Locate every blood parasite and identify its species.
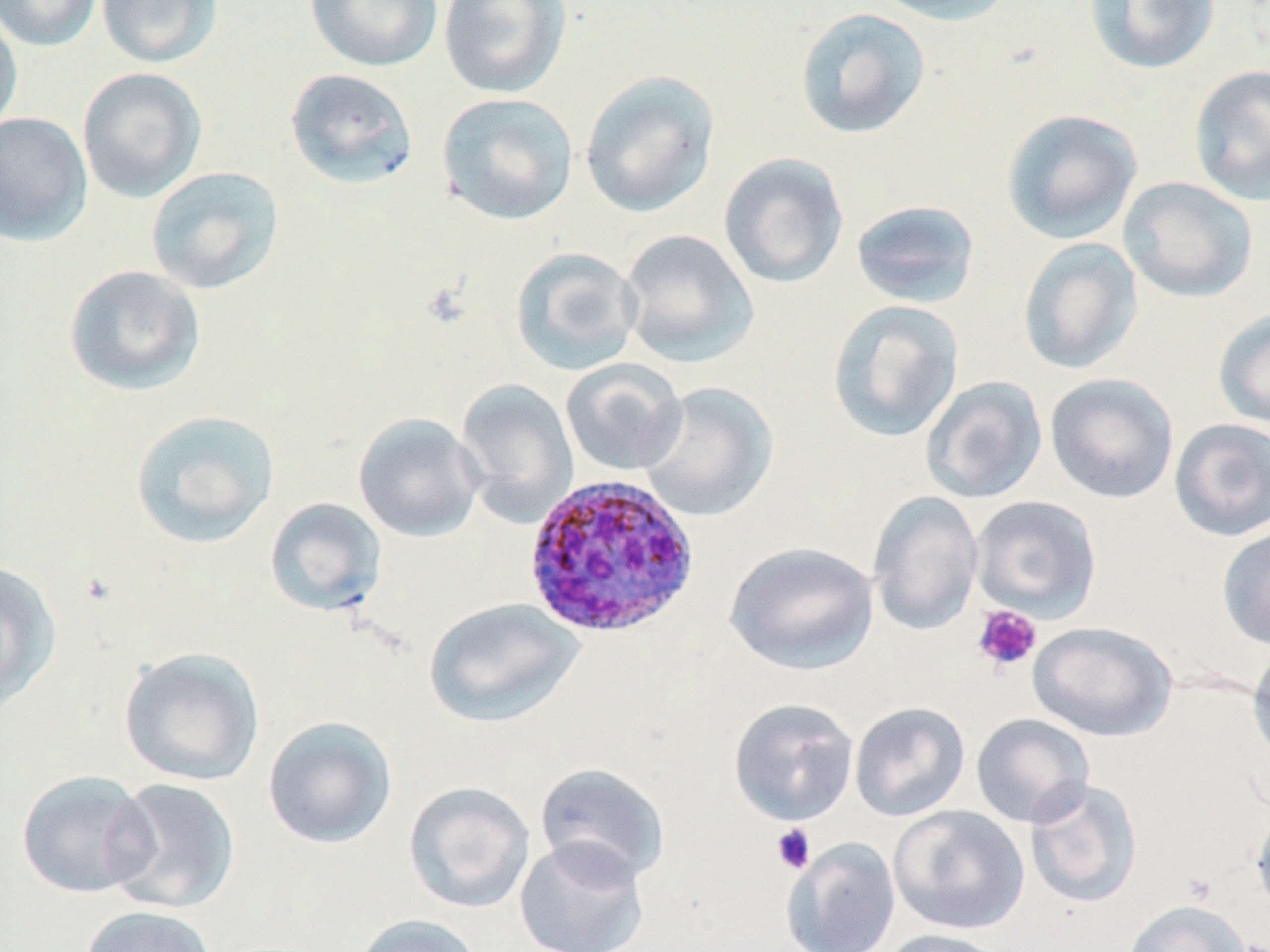

Approximate bounding boxes as (x1, y1, x2, y2) in pixels.
Plasmodium ovale-infected red blood cells: (522, 472, 701, 640).
No Plasmodium falciparum, Plasmodium malariae, Plasmodium vivax, Babesia divergens, or Trypanosoma brucei observed.

Summary:
  - Uninfected red blood cell locations: (0, 0, 102, 52), (96, 0, 223, 68), (305, 0, 442, 72), (438, 0, 571, 99), (869, 0, 1016, 26), (1084, 0, 1220, 75), (794, 7, 931, 140), (0, 11, 23, 135), (1188, 64, 1270, 206), (77, 67, 208, 203), (284, 67, 419, 190), (580, 70, 720, 218), (437, 92, 579, 225), (1000, 108, 1143, 245), (0, 112, 93, 246), (718, 152, 849, 289), (145, 167, 284, 295), (1118, 177, 1258, 303), (850, 200, 981, 309), (619, 229, 760, 369), (1017, 237, 1143, 375), (509, 246, 643, 376), (63, 265, 206, 396), (827, 299, 964, 443), (1213, 308, 1270, 429), (560, 359, 688, 476), (1044, 373, 1180, 505), (920, 375, 1048, 504), (455, 378, 579, 526), (638, 382, 778, 522), (129, 409, 280, 549), (353, 413, 486, 542), (1169, 418, 1270, 542), (868, 490, 984, 636), (970, 495, 1102, 622), (265, 497, 387, 618), (1216, 524, 1270, 651), (724, 541, 879, 676), (0, 560, 62, 712), (424, 597, 584, 728), (1028, 620, 1177, 741), (1247, 642, 1270, 769), (118, 647, 266, 787), (728, 698, 860, 826), (849, 702, 971, 822), (971, 713, 1095, 828), (262, 716, 397, 850), (535, 762, 671, 886), (15, 770, 157, 899), (102, 777, 241, 915), (1024, 778, 1144, 908), (403, 781, 536, 914), (888, 804, 1029, 935), (1250, 804, 1270, 917), (514, 836, 650, 952), (781, 837, 901, 952), (1122, 899, 1251, 952), (79, 905, 218, 952), (352, 914, 487, 952), (875, 928, 1010, 952)
  - Platelet locations: (971, 604, 1042, 674), (771, 824, 816, 874)
  - Slide-level diagnosis: Plasmodium ovale
  - Stain: May-Grünwald-Giemsa
  - Preparation: thin blood smear
  - Field of view: one of a larger specimen
  - Image size: 1270×952 pixels
  - Modality: optical microscopy
  - Magnification: 1000x